Look for Plasmodium parasites.
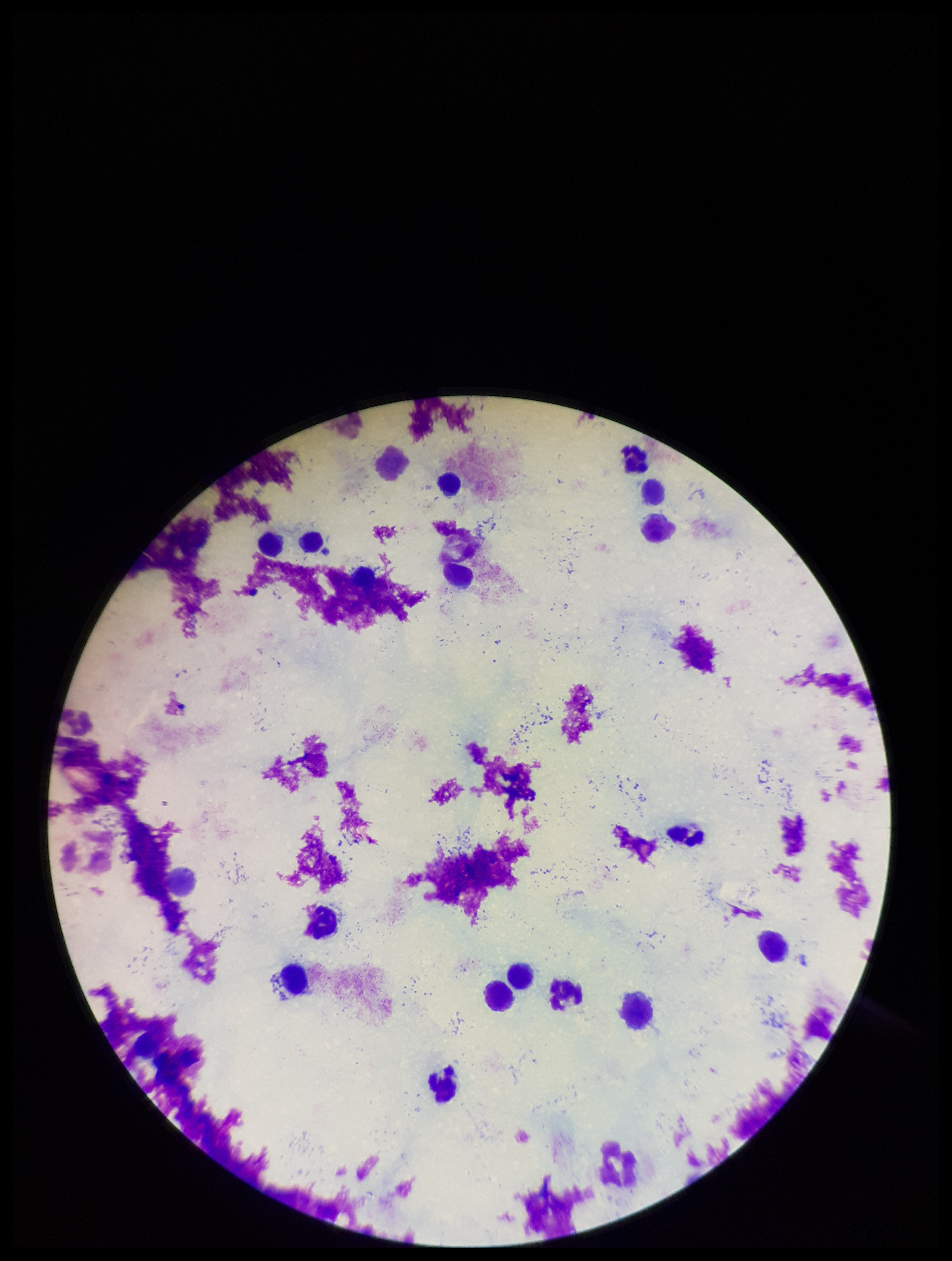
None identified.

Patient malaria status: negative. Smartphone photograph taken through the eyepiece of a microscope. Giemsa stain. Parasite count: 0. Leukocyte count: 17. Image is 952×1261 pixels. Preparation: thick smear. Single field of view.